Locate every blood parasite and identify its species.
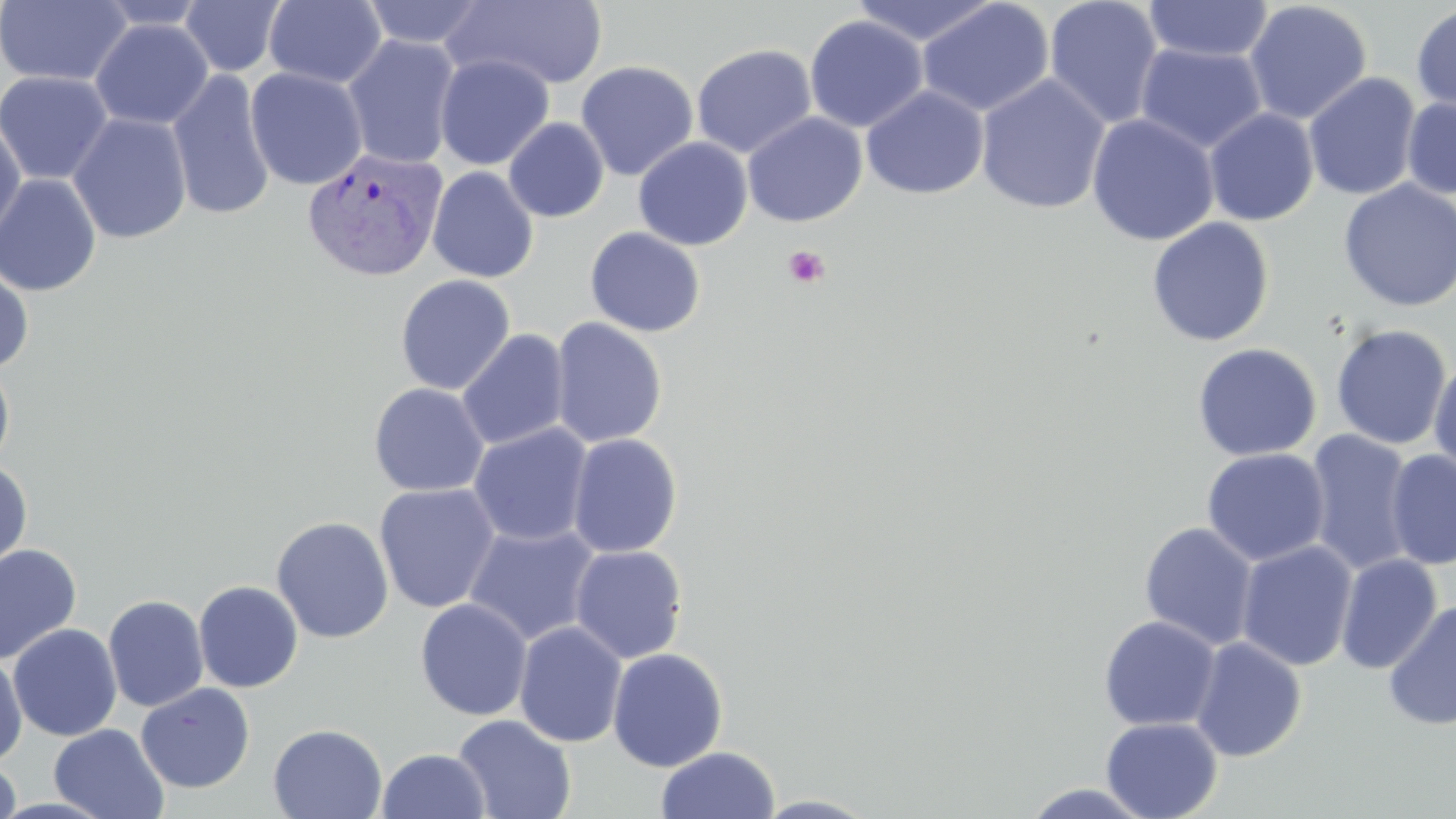

Approximate bounding boxes as named x1/y1/x2/y2 corners in pixels.
Plasmodium vivax-infected red blood cells: (x1=302, y1=147, x2=448, y2=282).
No Plasmodium falciparum, Plasmodium ovale, Plasmodium malariae, Babesia divergens, or Trypanosoma brucei observed.

slide-level diagnosis = Plasmodium vivax
platelet locations = approximate bounding boxes as named x1/y1/x2/y2 corners in pixels: (x1=783, y1=245, x2=830, y2=289)
image size = 1456×819 pixels
preparation = thin blood film
stain = May-Grünwald-Giemsa
magnification = 1000x
field of view = single
modality = optical microscopy
uninfected red blood cell locations = approximate bounding boxes as named x1/y1/x2/y2 corners in pixels: (x1=0, y1=0, x2=132, y2=87), (x1=179, y1=0, x2=287, y2=77), (x1=263, y1=0, x2=387, y2=88), (x1=360, y1=0, x2=490, y2=49), (x1=444, y1=0, x2=609, y2=91), (x1=849, y1=0, x2=1001, y2=47), (x1=1043, y1=0, x2=1164, y2=129), (x1=93, y1=1, x2=212, y2=31), (x1=916, y1=1, x2=1055, y2=117), (x1=1142, y1=1, x2=1275, y2=64), (x1=1244, y1=1, x2=1372, y2=125), (x1=1412, y1=3, x2=1456, y2=115), (x1=804, y1=16, x2=928, y2=132), (x1=89, y1=19, x2=214, y2=130), (x1=342, y1=34, x2=461, y2=170), (x1=691, y1=43, x2=817, y2=158), (x1=1136, y1=43, x2=1266, y2=154), (x1=434, y1=54, x2=554, y2=171), (x1=576, y1=60, x2=698, y2=181), (x1=245, y1=67, x2=368, y2=191), (x1=167, y1=69, x2=276, y2=221), (x1=0, y1=70, x2=115, y2=186), (x1=1303, y1=72, x2=1422, y2=201), (x1=975, y1=74, x2=1110, y2=214), (x1=861, y1=86, x2=989, y2=200), (x1=1402, y1=96, x2=1456, y2=198), (x1=1203, y1=108, x2=1319, y2=227), (x1=742, y1=112, x2=867, y2=227), (x1=67, y1=113, x2=192, y2=244), (x1=1086, y1=113, x2=1219, y2=246), (x1=0, y1=116, x2=27, y2=244), (x1=504, y1=117, x2=609, y2=222), (x1=633, y1=137, x2=753, y2=251), (x1=427, y1=166, x2=539, y2=283), (x1=0, y1=174, x2=102, y2=297), (x1=1338, y1=180, x2=1456, y2=312), (x1=1147, y1=217, x2=1274, y2=347), (x1=585, y1=227, x2=706, y2=337), (x1=0, y1=261, x2=35, y2=373), (x1=395, y1=275, x2=516, y2=395), (x1=549, y1=317, x2=668, y2=449), (x1=1329, y1=324, x2=1453, y2=450), (x1=457, y1=329, x2=570, y2=450), (x1=1192, y1=343, x2=1321, y2=462), (x1=1428, y1=353, x2=1456, y2=479), (x1=0, y1=359, x2=16, y2=473), (x1=369, y1=382, x2=489, y2=497), (x1=469, y1=423, x2=593, y2=546), (x1=1304, y1=431, x2=1416, y2=576), (x1=567, y1=433, x2=683, y2=558), (x1=1201, y1=448, x2=1330, y2=566), (x1=1385, y1=449, x2=1456, y2=571), (x1=0, y1=462, x2=33, y2=574), (x1=374, y1=483, x2=500, y2=614), (x1=271, y1=515, x2=394, y2=643), (x1=1139, y1=522, x2=1259, y2=650), (x1=464, y1=523, x2=601, y2=646), (x1=1236, y1=540, x2=1358, y2=672), (x1=0, y1=543, x2=82, y2=665), (x1=569, y1=545, x2=688, y2=664), (x1=1336, y1=553, x2=1442, y2=674), (x1=193, y1=580, x2=303, y2=693), (x1=103, y1=594, x2=209, y2=712), (x1=414, y1=598, x2=533, y2=721), (x1=1383, y1=601, x2=1456, y2=730), (x1=1098, y1=616, x2=1221, y2=731), (x1=513, y1=621, x2=628, y2=748), (x1=7, y1=623, x2=122, y2=741), (x1=1190, y1=637, x2=1307, y2=761), (x1=607, y1=648, x2=729, y2=771), (x1=0, y1=651, x2=27, y2=766), (x1=135, y1=682, x2=255, y2=793), (x1=452, y1=714, x2=577, y2=819), (x1=1100, y1=717, x2=1223, y2=819), (x1=268, y1=723, x2=387, y2=818), (x1=49, y1=724, x2=169, y2=819), (x1=655, y1=746, x2=780, y2=819), (x1=377, y1=748, x2=490, y2=819), (x1=0, y1=758, x2=21, y2=819), (x1=1019, y1=783, x2=1158, y2=818), (x1=750, y1=794, x2=881, y2=818)